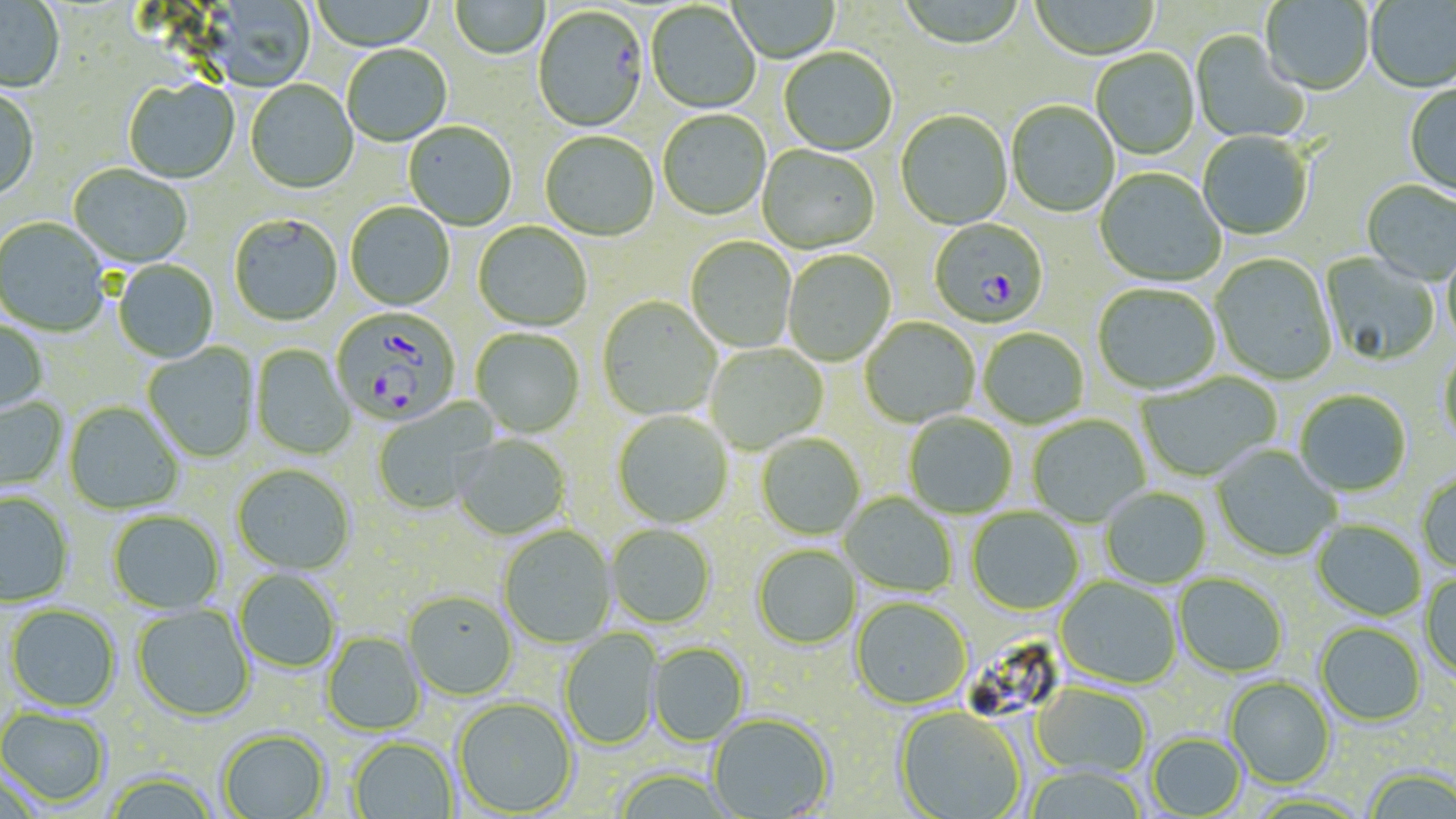

plasmodium_falciparum_infected_red_blood_cell_locations: 'approximate bounding boxes as (x1, y1, x2, y2) in pixels: (533, 7, 648, 134), (929, 220, 1049, 330), (333, 311, 463, 430)'
slide_level_diagnosis: Plasmodium falciparum
field_of_view: single
image_size: 1456×819 pixels
modality: optical microscopy
stain: May-Grünwald-Giemsa
uninfected_red_blood_cell_locations: 'approximate bounding boxes as (x1, y1, x2, y2) in pixels: (310, 0, 438, 52), (896, 0, 1027, 52), (1030, 0, 1160, 61), (0, 1, 65, 95), (202, 1, 316, 93), (450, 1, 550, 60), (727, 1, 840, 64), (1260, 1, 1374, 97), (1365, 1, 1456, 94), (646, 3, 760, 115), (1190, 31, 1310, 144), (342, 45, 452, 147), (778, 49, 898, 157), (1091, 50, 1200, 161), (124, 79, 240, 185), (245, 80, 358, 195), (1404, 84, 1456, 200), (0, 90, 39, 202), (1005, 102, 1119, 218), (658, 111, 771, 221), (895, 112, 1012, 231), (403, 123, 516, 231), (540, 132, 659, 242), (1197, 132, 1313, 240), (757, 145, 880, 255), (68, 165, 193, 270), (1094, 169, 1225, 288), (1361, 181, 1456, 286), (345, 203, 455, 311), (229, 215, 342, 328), (0, 219, 110, 337), (472, 222, 592, 332), (686, 238, 797, 353), (1443, 243, 1456, 351), (783, 251, 896, 366), (1319, 253, 1441, 367), (1211, 254, 1337, 386), (113, 260, 219, 364), (1093, 285, 1221, 395), (597, 297, 722, 421), (860, 318, 980, 428), (0, 320, 48, 417), (471, 329, 584, 438), (978, 329, 1088, 429), (142, 343, 260, 464), (705, 343, 828, 454), (250, 345, 356, 460), (1439, 345, 1456, 450), (1137, 372, 1281, 482), (1295, 391, 1412, 498), (0, 396, 69, 493), (372, 400, 497, 516), (64, 403, 183, 515), (613, 411, 733, 528), (904, 412, 1017, 519), (1027, 416, 1151, 527), (453, 434, 571, 540), (756, 434, 865, 541), (1210, 445, 1342, 562), (231, 465, 355, 576), (1416, 472, 1456, 574), (1100, 487, 1211, 589), (0, 493, 74, 607), (840, 493, 957, 596), (967, 507, 1083, 615), (107, 511, 225, 616), (1311, 520, 1426, 621), (606, 524, 716, 629), (497, 526, 617, 649), (752, 544, 862, 650), (234, 570, 340, 673), (1174, 573, 1288, 678), (1420, 574, 1456, 683), (1056, 578, 1181, 689), (403, 590, 518, 701), (850, 597, 972, 710), (132, 604, 255, 722), (5, 605, 120, 713), (1315, 623, 1427, 727), (559, 628, 663, 751), (321, 632, 426, 736), (648, 643, 749, 747), (1224, 676, 1337, 789), (1031, 683, 1152, 778), (452, 697, 578, 816), (0, 707, 111, 808), (894, 707, 1027, 819), (707, 713, 835, 817), (217, 728, 330, 819), (1146, 732, 1247, 818), (349, 737, 458, 819), (1025, 767, 1147, 819), (1363, 768, 1455, 818), (609, 769, 736, 818), (0, 772, 46, 819), (103, 773, 219, 819)'
magnification: 1000x
preparation: thin blood film